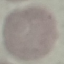
malaria status = uninfected
image type = automatically extracted cell patch, resized to 64 × 64 pixels
preparation = thin blood smear
capture = smartphone camera at the microscope eyepiece
stain = Giemsa